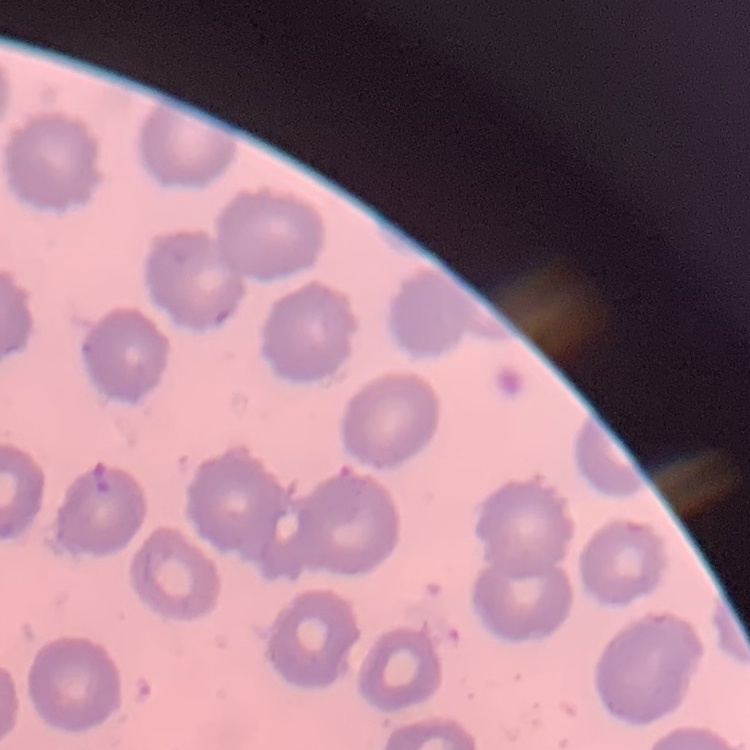
erythrocyte morphology = no rouleaux formation
stain = Field's or Giemsa
image type = one tile cut from a larger photomicrograph
preparation = thin blood film